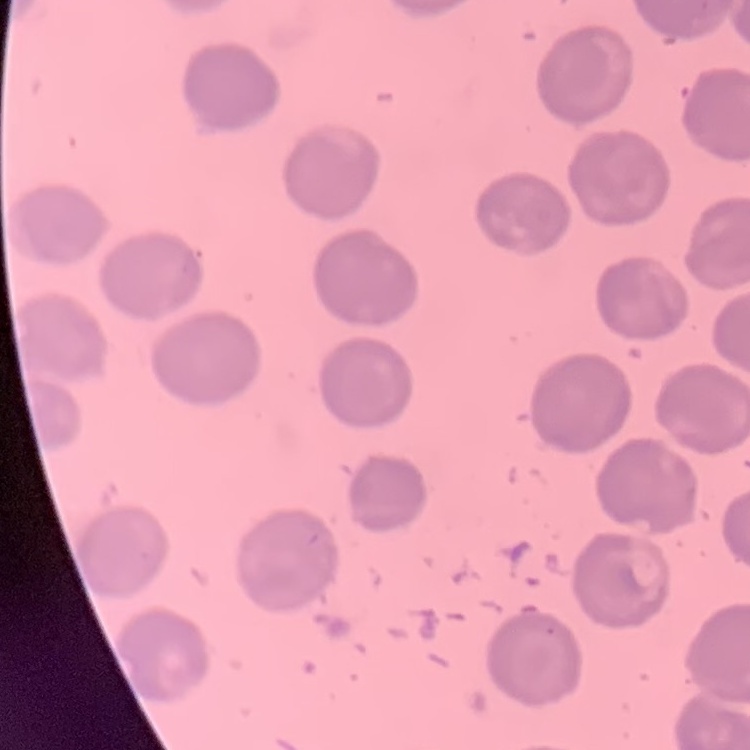
red blood cell morphology = no rouleaux formation
image type = square crop of a larger photomicrograph
stain = Field's or Giemsa
preparation = thin peripheral smear